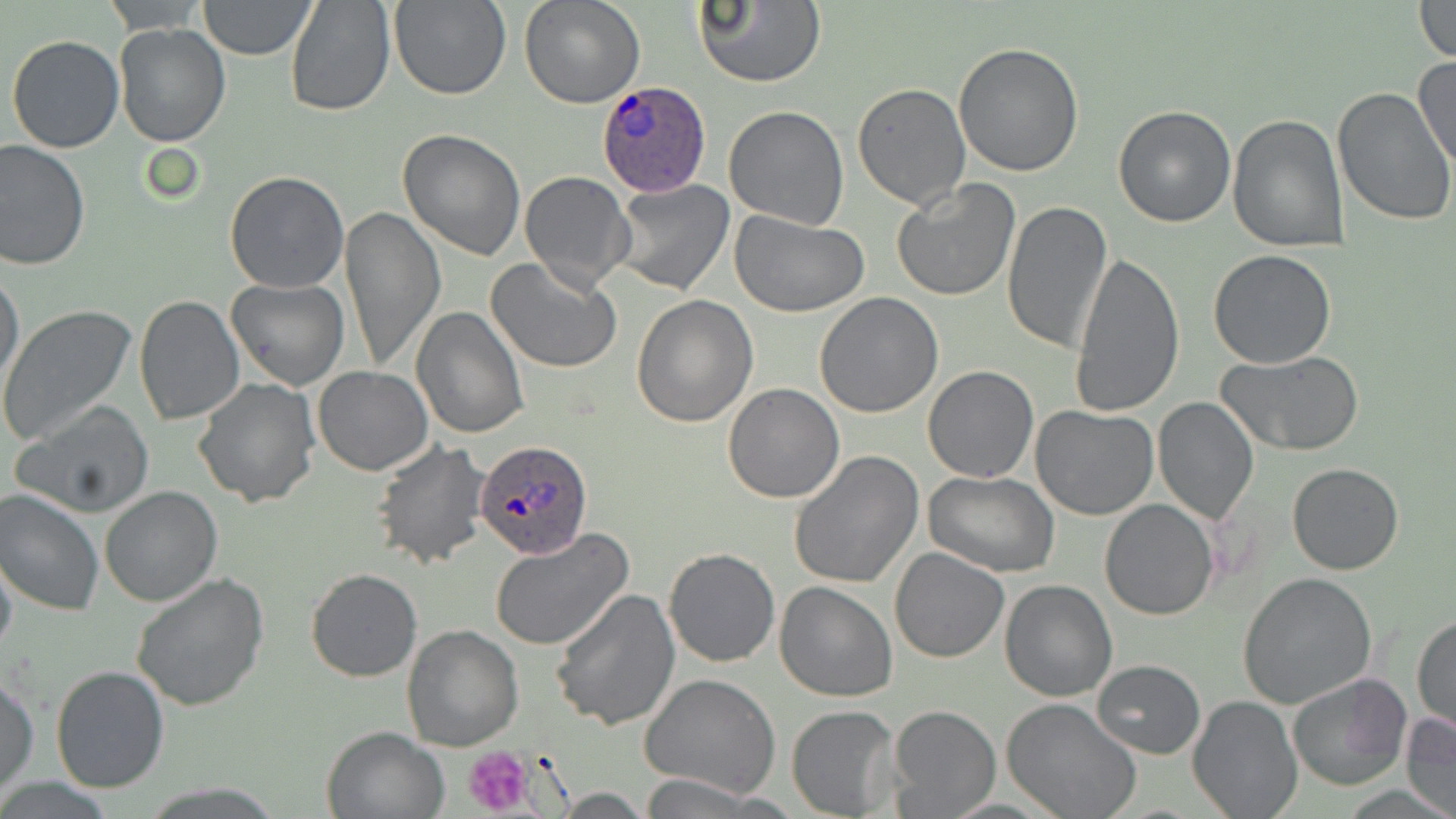

{
  "plasmodium_ovale_infected_red_blood_cell_locations": "approximate bounding boxes as [x1, y1, x2, y2] in pixels: [594, 80, 713, 197], [475, 438, 592, 561]",
  "slide_level_diagnosis": "Plasmodium ovale",
  "stain": "May-Grünwald-Giemsa",
  "magnification": "1000x",
  "modality": "light microscopy",
  "field_of_view": "one of a larger specimen",
  "uninfected_red_blood_cell_locations": "approximate bounding boxes as [x1, y1, x2, y2] in pixels: [285, 0, 396, 118], [388, 0, 510, 101], [519, 0, 645, 109], [692, 0, 824, 88], [101, 1, 210, 33], [198, 1, 317, 59], [1411, 1, 1456, 63], [114, 23, 231, 148], [6, 34, 125, 154], [953, 43, 1085, 178], [1413, 54, 1456, 174], [853, 82, 971, 212], [1332, 88, 1456, 229], [723, 105, 851, 230], [1111, 105, 1237, 228], [1227, 113, 1348, 251], [398, 128, 527, 261], [0, 139, 91, 270], [519, 171, 635, 292], [224, 172, 349, 294], [610, 179, 736, 297], [892, 179, 1021, 302], [1001, 199, 1113, 356], [339, 206, 445, 372], [728, 209, 870, 316], [1069, 249, 1186, 420], [1207, 249, 1337, 369], [488, 256, 623, 373], [0, 269, 24, 393], [225, 278, 348, 391], [815, 293, 944, 417], [631, 295, 759, 428], [133, 297, 244, 425], [409, 305, 529, 439], [0, 306, 136, 447], [1216, 351, 1365, 455], [921, 365, 1038, 483], [313, 366, 432, 476], [192, 376, 320, 507], [722, 382, 845, 503], [1153, 396, 1258, 523], [12, 401, 156, 518], [1030, 404, 1158, 520], [370, 440, 492, 570], [788, 451, 924, 589], [1288, 462, 1405, 575], [924, 472, 1062, 578], [101, 485, 221, 606], [0, 489, 104, 617], [1099, 499, 1219, 621], [490, 528, 634, 652], [663, 546, 781, 667], [889, 547, 1010, 663], [0, 549, 17, 660], [304, 569, 421, 681], [131, 572, 269, 711], [1237, 572, 1376, 710], [1000, 579, 1118, 701], [772, 582, 897, 702], [548, 588, 679, 730], [1412, 614, 1455, 736], [402, 626, 524, 750], [1092, 659, 1205, 758], [50, 664, 170, 793], [1286, 672, 1413, 791], [1, 674, 39, 794], [640, 674, 780, 799], [1188, 695, 1301, 818], [1000, 697, 1143, 819], [787, 705, 901, 817], [886, 705, 1001, 817], [1401, 712, 1456, 818], [321, 726, 449, 819], [636, 774, 773, 817]",
  "image_size": "1456×819 pixels",
  "preparation": "thin blood film",
  "platelet_locations": "approximate bounding boxes as [x1, y1, x2, y2] in pixels: [462, 745, 538, 816]"
}